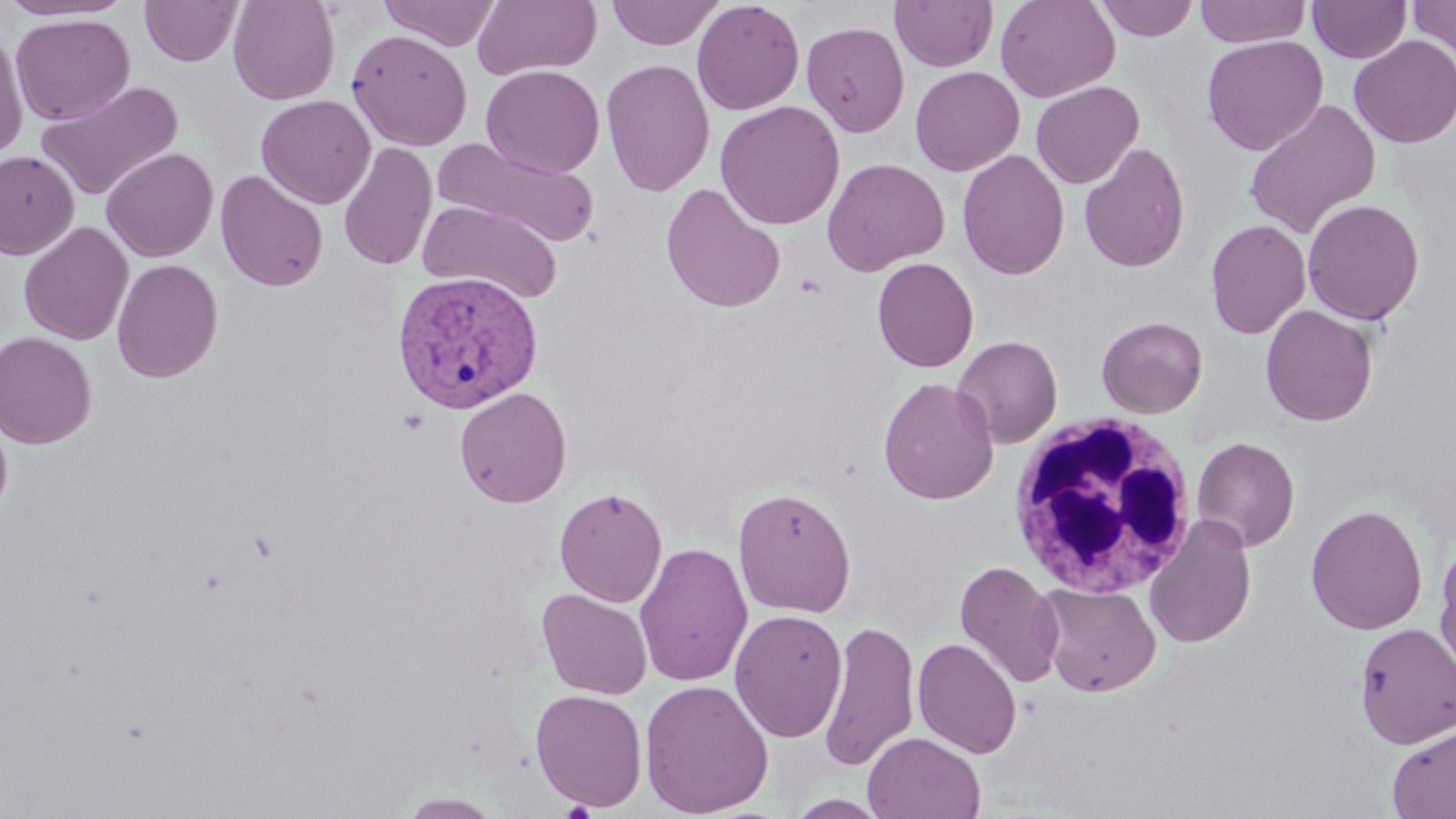

Summary:
  - Coordinate format: approximate bounding boxes as (x1, y1, x2, y2) in pixels
  - Plasmodium vivax-infected red blood cell locations: (393, 269, 543, 414)
  - White blood cell locations: (1007, 411, 1199, 600)
  - Uninfected red blood cell locations: (0, 0, 131, 21), (140, 0, 242, 66), (228, 0, 340, 105), (378, 0, 501, 50), (473, 0, 602, 82), (605, 0, 725, 49), (692, 0, 805, 116), (890, 0, 998, 72), (995, 0, 1120, 102), (1094, 0, 1199, 41), (1194, 0, 1311, 47), (1307, 0, 1412, 63), (1407, 0, 1456, 65), (11, 13, 135, 126), (801, 21, 910, 138), (0, 25, 29, 161), (347, 29, 473, 151), (1202, 35, 1328, 155), (1349, 35, 1456, 148), (601, 58, 716, 197), (481, 64, 604, 178), (910, 65, 1025, 176), (35, 80, 183, 202), (1031, 80, 1144, 188), (256, 94, 376, 208), (1243, 98, 1381, 238), (715, 100, 845, 230), (434, 138, 599, 248), (338, 141, 437, 271), (1078, 142, 1190, 273), (101, 147, 218, 263), (957, 149, 1070, 279), (0, 150, 80, 259), (822, 157, 949, 276), (214, 170, 329, 291), (661, 182, 786, 313), (1302, 198, 1424, 326), (419, 199, 563, 304), (1206, 219, 1311, 339), (19, 222, 133, 345), (872, 257, 979, 373), (112, 258, 223, 383), (1261, 304, 1378, 426), (1097, 316, 1208, 418), (0, 331, 97, 449), (952, 335, 1063, 448), (878, 377, 999, 504), (455, 387, 572, 508), (0, 410, 13, 525), (1192, 436, 1300, 551), (554, 486, 668, 607), (733, 487, 856, 618), (1305, 504, 1428, 635), (1144, 513, 1257, 649), (1434, 539, 1456, 676), (634, 541, 753, 686), (955, 560, 1065, 689), (1034, 582, 1162, 697), (537, 588, 653, 699), (729, 609, 848, 744), (819, 617, 920, 772), (1354, 622, 1456, 748), (913, 637, 1023, 759), (639, 678, 774, 817), (531, 688, 648, 811), (1386, 723, 1456, 819), (862, 731, 986, 818), (398, 791, 505, 818), (783, 793, 892, 818)
  - Slide-level diagnosis: Plasmodium vivax
  - Modality: optical microscopy
  - Image size: 1456×819 pixels
  - Field of view: single
  - Stain: May-Grünwald-Giemsa
  - Magnification: 1000x
  - Preparation: thin blood film